Locate every Plasmodium falciparum-infected red blood cell.
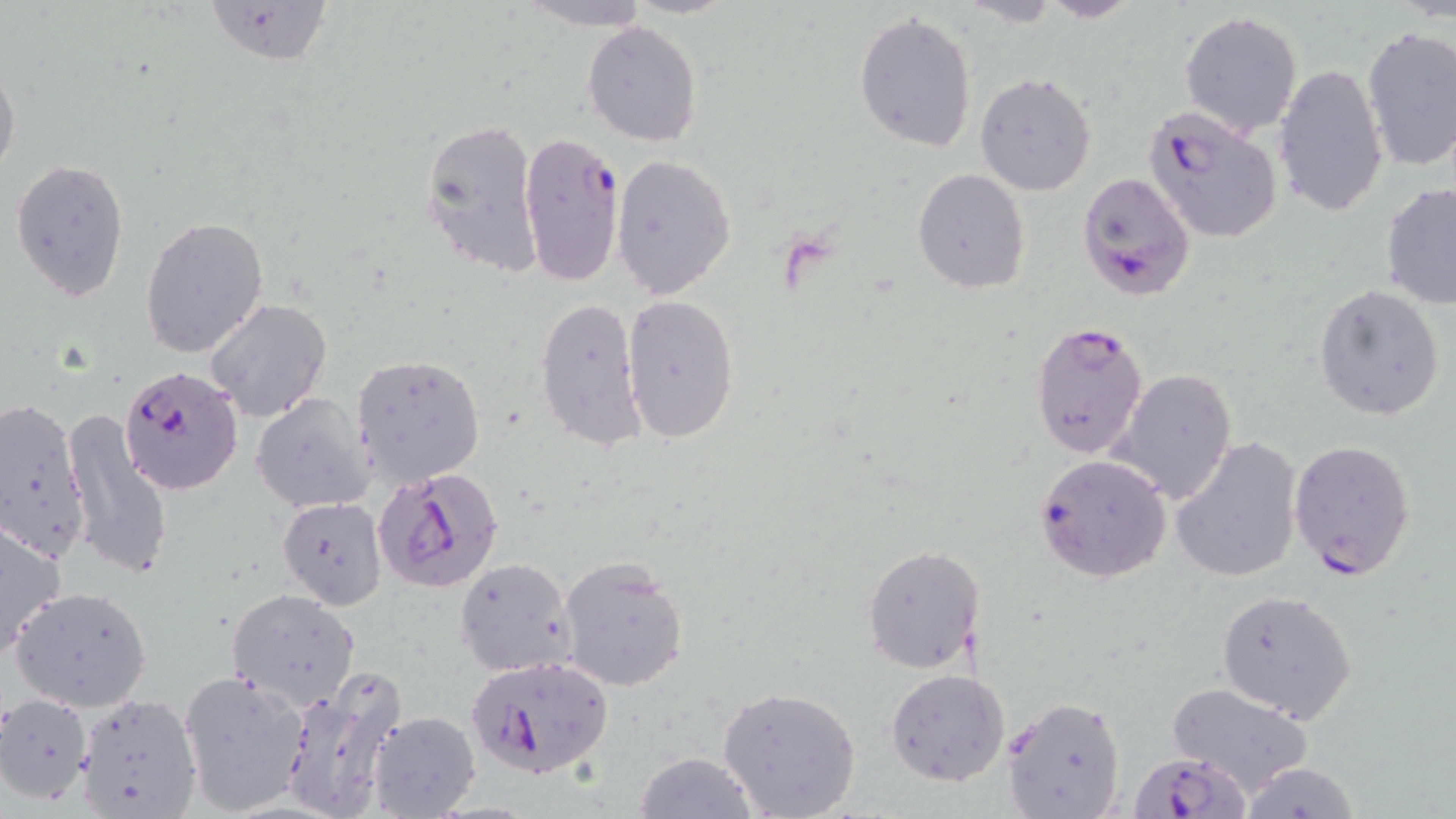
Approximate bounding boxes as named x1/y1/x2/y2 corners in pixels.
Plasmodium falciparum-infected red blood cells: (x1=1141, y1=104, x2=1284, y2=245), (x1=518, y1=135, x2=623, y2=288), (x1=1076, y1=172, x2=1195, y2=301), (x1=1029, y1=320, x2=1149, y2=461), (x1=119, y1=363, x2=245, y2=496), (x1=1288, y1=438, x2=1417, y2=582), (x1=1033, y1=454, x2=1172, y2=583), (x1=373, y1=465, x2=504, y2=593), (x1=462, y1=653, x2=614, y2=781), (x1=1131, y1=749, x2=1248, y2=818).

Uninfected red blood cell locations: (x1=202, y1=0, x2=335, y2=71), (x1=517, y1=0, x2=656, y2=28), (x1=959, y1=0, x2=1063, y2=27), (x1=1035, y1=0, x2=1141, y2=23), (x1=853, y1=11, x2=978, y2=154), (x1=1179, y1=11, x2=1303, y2=137), (x1=583, y1=20, x2=702, y2=146), (x1=1360, y1=27, x2=1456, y2=173), (x1=0, y1=55, x2=22, y2=185), (x1=1274, y1=63, x2=1388, y2=218), (x1=975, y1=71, x2=1097, y2=196), (x1=418, y1=117, x2=543, y2=278), (x1=611, y1=154, x2=737, y2=300), (x1=10, y1=159, x2=130, y2=300), (x1=912, y1=168, x2=1030, y2=294), (x1=1380, y1=181, x2=1456, y2=309), (x1=140, y1=217, x2=270, y2=360), (x1=1311, y1=284, x2=1446, y2=421), (x1=622, y1=293, x2=741, y2=443), (x1=534, y1=295, x2=644, y2=452), (x1=206, y1=300, x2=331, y2=423), (x1=353, y1=353, x2=486, y2=487), (x1=1113, y1=368, x2=1237, y2=506), (x1=253, y1=393, x2=374, y2=513), (x1=0, y1=394, x2=94, y2=562), (x1=63, y1=411, x2=174, y2=581), (x1=1170, y1=435, x2=1302, y2=584), (x1=276, y1=497, x2=386, y2=609), (x1=0, y1=518, x2=68, y2=657), (x1=860, y1=544, x2=984, y2=674), (x1=558, y1=556, x2=689, y2=691), (x1=455, y1=557, x2=577, y2=677), (x1=12, y1=586, x2=153, y2=711), (x1=226, y1=588, x2=363, y2=710), (x1=1216, y1=588, x2=1358, y2=722), (x1=885, y1=669, x2=1010, y2=788), (x1=178, y1=670, x2=312, y2=814), (x1=280, y1=675, x2=405, y2=819), (x1=1164, y1=680, x2=1317, y2=796), (x1=716, y1=684, x2=862, y2=818), (x1=0, y1=691, x2=93, y2=806), (x1=71, y1=692, x2=203, y2=819), (x1=1000, y1=695, x2=1126, y2=817), (x1=367, y1=710, x2=481, y2=818), (x1=634, y1=750, x2=763, y2=819), (x1=1236, y1=762, x2=1361, y2=818). Slide-level diagnosis: Plasmodium falciparum. Thin blood film. Light microscopy. May-Grünwald-Giemsa-stained preparation. Image is 1456×819 pixels. 1000x magnification. Single field of view.